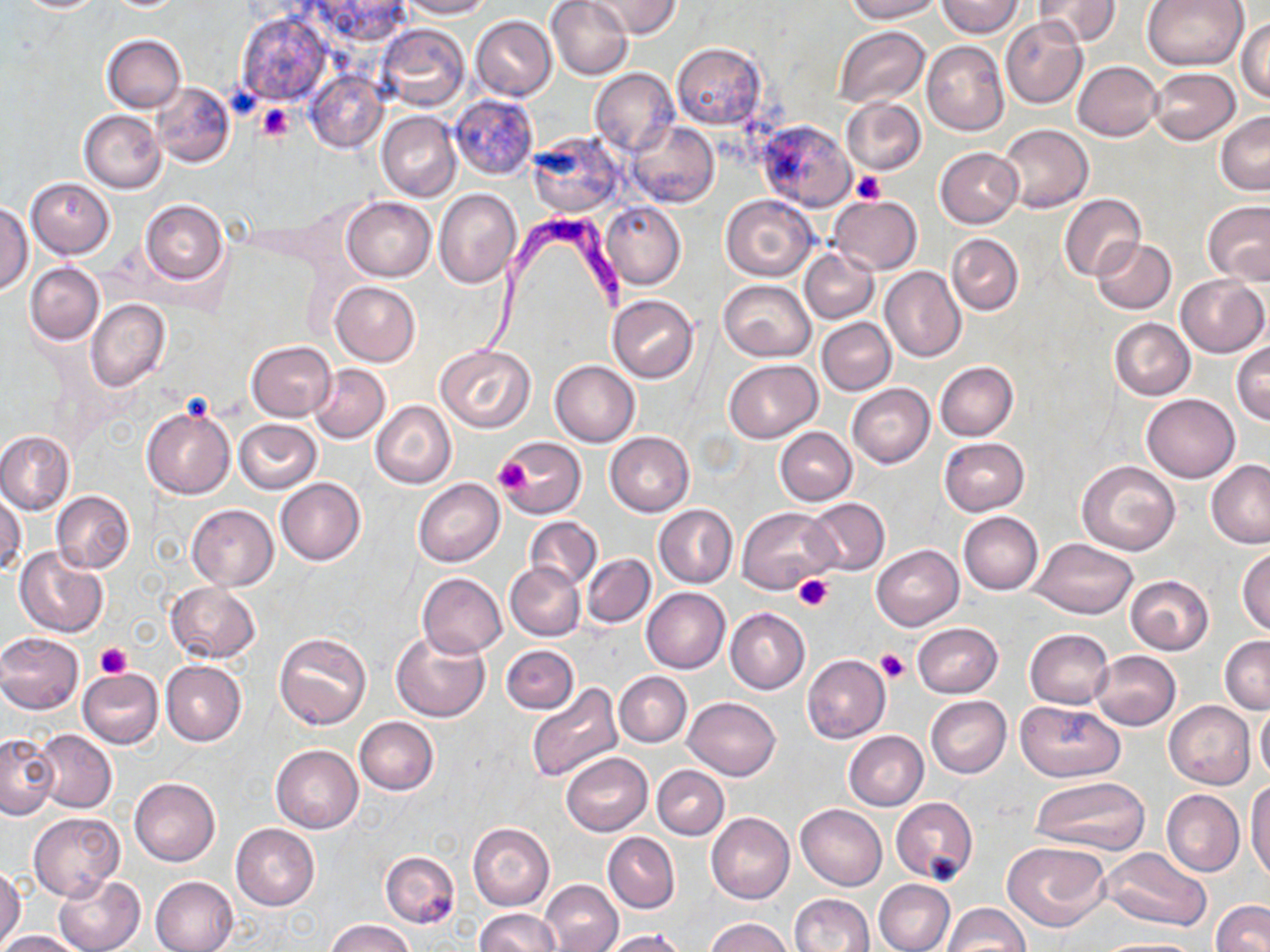

Summary:
  - Coordinate format: approximate bounding boxes as [x1, y1, x2, y2] in pixels
  - Trypanosoma brucei locations: [472, 207, 630, 366]
  - Platelet locations: [257, 104, 293, 141], [854, 170, 886, 205], [493, 454, 531, 497], [798, 575, 835, 611], [96, 643, 132, 679], [876, 649, 909, 683]
  - Uninfected red blood cell locations: [10, 0, 109, 12], [309, 0, 415, 43], [400, 0, 491, 19], [547, 0, 633, 79], [587, 0, 682, 39], [846, 0, 942, 22], [939, 0, 1022, 37], [1035, 0, 1119, 47], [1141, 0, 1249, 71], [237, 12, 330, 107], [1000, 15, 1087, 108], [471, 16, 557, 101], [1237, 16, 1270, 103], [376, 24, 470, 110], [833, 27, 930, 107], [103, 35, 186, 113], [922, 41, 1009, 136], [671, 43, 766, 129], [1073, 60, 1163, 141], [590, 68, 678, 156], [1149, 68, 1240, 145], [304, 72, 387, 153], [150, 83, 234, 167], [449, 94, 540, 182], [841, 97, 926, 176], [79, 110, 165, 192], [1215, 110, 1270, 196], [377, 111, 462, 201], [755, 119, 856, 211], [627, 121, 719, 208], [997, 123, 1093, 213], [525, 131, 626, 217], [935, 147, 1023, 228], [27, 179, 113, 258], [433, 189, 521, 288], [1059, 193, 1146, 282], [720, 194, 818, 281], [829, 196, 921, 274], [341, 198, 435, 282], [140, 199, 228, 285], [1202, 200, 1270, 285], [0, 201, 33, 295], [601, 201, 686, 289], [946, 233, 1024, 315], [1091, 238, 1175, 314], [800, 248, 878, 323], [26, 262, 104, 345], [881, 266, 966, 362], [31, 273, 156, 361], [1176, 275, 1268, 357], [718, 280, 815, 361], [331, 281, 420, 365], [607, 295, 700, 382], [87, 299, 170, 392], [816, 317, 895, 396], [1110, 318, 1196, 401], [247, 340, 337, 420], [1231, 340, 1270, 426], [435, 344, 535, 432], [549, 360, 640, 446], [724, 360, 821, 442], [934, 361, 1019, 440], [309, 363, 391, 443], [847, 384, 934, 468], [1141, 394, 1240, 483], [371, 401, 456, 488], [140, 405, 236, 500], [234, 419, 321, 494], [774, 427, 857, 505], [0, 430, 74, 515], [605, 432, 694, 516], [939, 436, 1029, 515], [498, 437, 586, 518], [1076, 460, 1180, 555], [1206, 460, 1270, 549], [276, 477, 365, 564], [413, 478, 505, 567], [1, 490, 25, 573], [52, 490, 134, 574], [804, 497, 890, 577], [186, 503, 279, 590], [655, 504, 736, 589], [738, 506, 838, 595], [958, 511, 1044, 595], [524, 517, 601, 591], [1029, 537, 1139, 618], [872, 544, 962, 630], [14, 546, 107, 638], [1237, 547, 1270, 635], [582, 554, 655, 627], [505, 562, 584, 641], [418, 573, 507, 657], [1126, 575, 1213, 654], [166, 582, 262, 663], [642, 588, 731, 674], [725, 607, 810, 693], [912, 622, 1003, 698], [1023, 629, 1113, 710], [391, 630, 489, 723], [275, 631, 371, 729], [0, 632, 84, 713], [1219, 635, 1269, 714], [501, 645, 579, 714], [1089, 650, 1182, 730], [802, 654, 890, 743], [161, 660, 246, 746], [77, 668, 163, 749], [615, 671, 691, 748], [525, 682, 624, 784], [925, 695, 1011, 778], [683, 696, 780, 780], [1015, 701, 1125, 781], [1164, 701, 1254, 789], [1255, 703, 1270, 782], [354, 717, 439, 795], [34, 729, 117, 813], [843, 731, 928, 810], [0, 735, 59, 819], [271, 745, 363, 833], [562, 752, 652, 835], [653, 764, 729, 840], [130, 777, 221, 866], [1029, 777, 1150, 856], [1247, 779, 1270, 882], [1161, 789, 1244, 877], [891, 797, 978, 883], [796, 804, 887, 889], [28, 812, 123, 900], [707, 812, 794, 904], [468, 822, 555, 911], [230, 823, 320, 910], [603, 832, 680, 913], [1003, 839, 1112, 930], [1102, 846, 1211, 931], [380, 851, 460, 927], [0, 865, 26, 947], [53, 875, 145, 952], [150, 875, 238, 952], [874, 878, 955, 952], [539, 879, 623, 952], [789, 893, 874, 952], [1210, 900, 1270, 952], [943, 902, 1029, 950], [474, 908, 562, 951], [705, 918, 792, 952], [325, 919, 415, 952], [602, 929, 687, 952], [0, 931, 84, 952], [1094, 938, 1204, 952]
  - Slide-level diagnosis: Trypanosoma brucei
  - Magnification: 1000x
  - Image size: 1270×952 pixels
  - Preparation: thin blood smear
  - Stain: May-Grünwald-Giemsa
  - Modality: optical microscopy
  - Field of view: one of a larger specimen